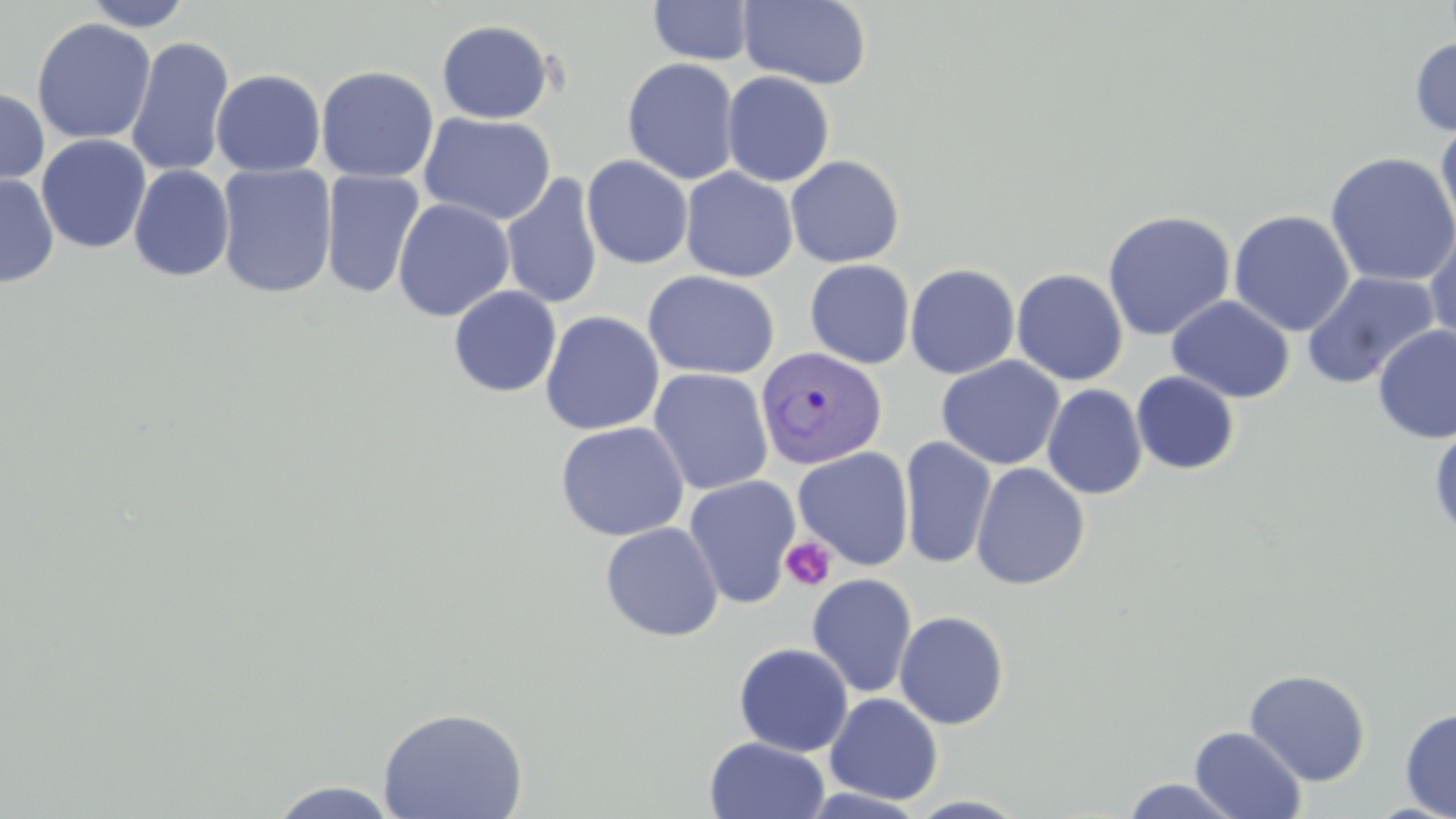
Approximate bounding boxes as (x1,y1)-(x2,y2) corner pairs in pixels. Platelet locations: (781,536)-(836,592). Plasmodium vivax-infected red blood cell locations: (754,345)-(889,469). Uninfected red blood cell locations: (82,0)-(195,31), (738,0)-(872,90), (648,1)-(754,66), (31,18)-(156,145), (436,19)-(555,124), (125,36)-(234,179), (1409,37)-(1456,137), (622,57)-(740,184), (315,65)-(440,183), (211,69)-(326,177), (721,71)-(835,187), (0,85)-(51,196), (419,112)-(557,226), (1435,119)-(1456,238), (36,134)-(152,254), (1324,152)-(1456,288), (581,155)-(693,269), (785,155)-(905,268), (128,164)-(235,282), (216,164)-(338,299), (680,167)-(798,282), (321,169)-(425,299), (500,173)-(604,310), (0,174)-(59,288), (392,198)-(515,322), (1102,209)-(1236,341), (1229,210)-(1355,337), (1424,226)-(1456,349), (805,260)-(915,369), (905,263)-(1021,379), (1011,268)-(1129,386), (642,270)-(780,380), (1301,271)-(1440,389), (448,286)-(562,397), (1166,295)-(1295,403), (540,311)-(665,435), (1372,324)-(1456,445), (937,356)-(1064,470), (648,368)-(773,496), (1131,371)-(1240,475), (1042,384)-(1148,500), (554,421)-(689,541), (1429,426)-(1456,541), (899,435)-(997,570), (792,446)-(914,571), (970,462)-(1090,590), (683,476)-(801,608), (600,522)-(725,643), (806,573)-(917,698), (894,610)-(1010,729), (733,642)-(853,757), (1244,668)-(1371,786), (825,692)-(944,805), (377,707)-(528,819), (1399,707)-(1456,819), (1189,726)-(1307,818), (704,736)-(830,819), (1120,777)-(1243,818), (269,780)-(400,818). Slide-level diagnosis: Plasmodium vivax. Thin blood film. 1000x magnification. May-Grünwald-Giemsa-stained preparation. Image is 1456×819 pixels. Optical microscopy. Single field of view.